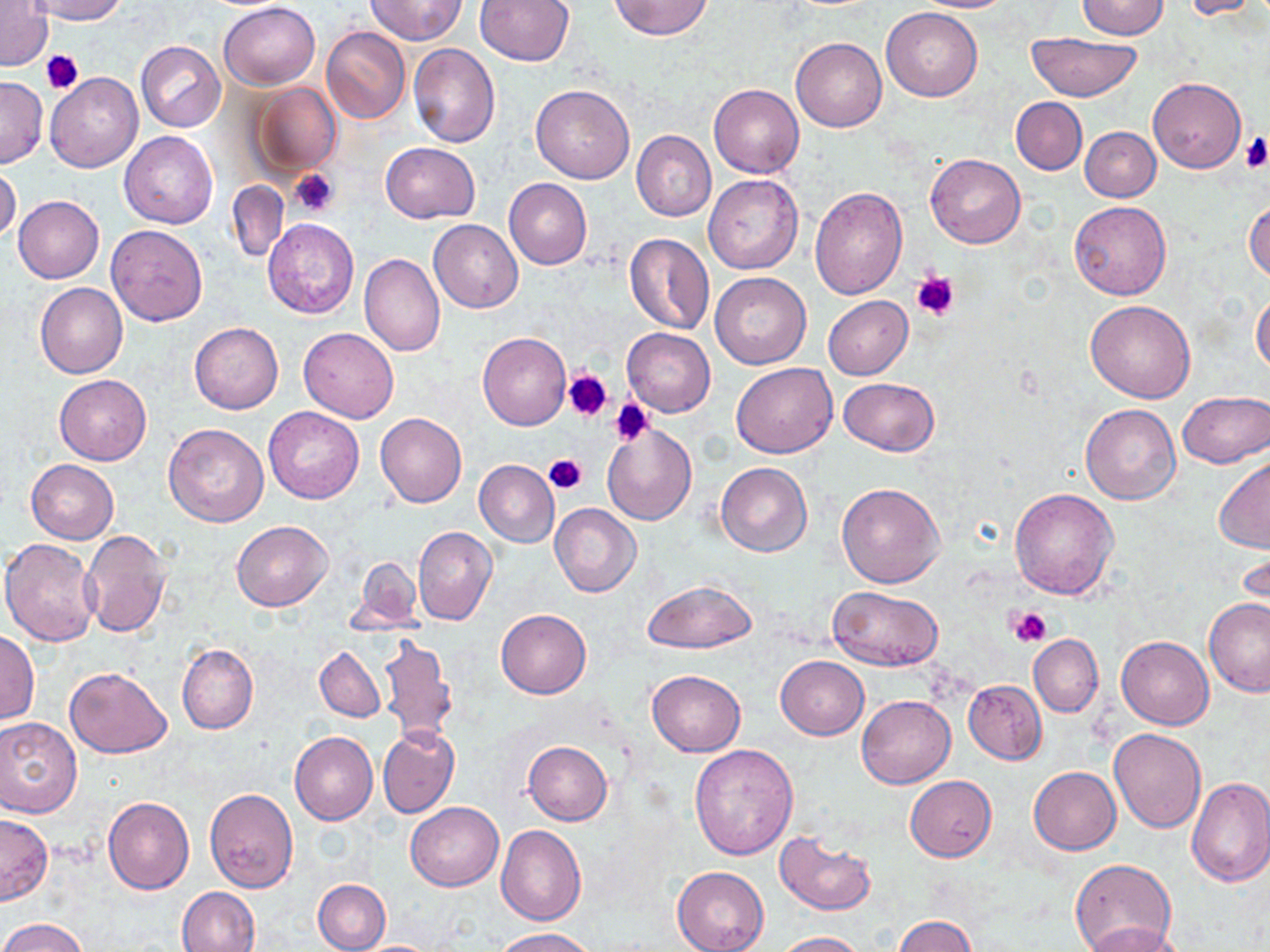

Summary:
  - Coordinate format: approximate bounding boxes as (x1,y1)-(x2,y2) corner pairs in pixels
  - Uninfected red blood cell locations: (23,0)-(128,24), (365,0)-(468,45), (474,0)-(575,66), (911,0)-(1014,12), (1075,0)-(1169,40), (1178,0)-(1264,19), (609,1)-(713,39), (1,2)-(53,73), (219,3)-(320,90), (883,8)-(982,101), (321,26)-(411,124), (1025,32)-(1142,100), (791,37)-(887,132), (135,40)-(226,132), (408,44)-(500,148), (44,73)-(142,173), (0,76)-(47,167), (1148,77)-(1245,172), (250,83)-(340,177), (531,83)-(634,183), (710,84)-(804,178), (1010,97)-(1086,174), (1081,127)-(1161,201), (119,131)-(218,228), (631,131)-(716,221), (380,142)-(482,224), (926,153)-(1026,249), (0,165)-(21,244), (705,175)-(804,275), (504,178)-(591,270), (226,180)-(288,263), (810,185)-(908,299), (14,195)-(104,283), (1245,198)-(1270,284), (1068,200)-(1172,300), (263,217)-(360,318), (428,218)-(523,312), (105,225)-(208,326), (624,233)-(714,335), (359,254)-(445,357), (709,271)-(812,370), (36,282)-(128,378), (1252,290)-(1270,377), (823,296)-(912,379), (1085,299)-(1196,403), (190,323)-(283,414), (298,328)-(398,422), (623,328)-(716,416), (478,331)-(571,430), (732,362)-(838,457), (53,374)-(152,465), (838,377)-(938,457), (1178,390)-(1270,468), (1080,404)-(1181,505), (263,407)-(364,504), (375,412)-(466,508), (163,422)-(269,527), (602,424)-(697,525), (1215,456)-(1270,551), (25,459)-(119,543), (474,460)-(559,546), (715,462)-(812,558), (836,483)-(945,588), (1009,487)-(1121,599), (550,503)-(642,597), (231,521)-(332,611), (413,526)-(497,625), (80,529)-(172,638), (2,537)-(102,646), (1237,542)-(1269,629), (353,557)-(424,630), (643,579)-(756,654), (828,587)-(942,671), (1203,597)-(1270,695), (495,609)-(591,699), (0,631)-(38,724), (1028,634)-(1103,716), (378,635)-(457,746), (1115,635)-(1213,731), (178,645)-(258,734), (315,645)-(386,722), (775,655)-(868,739), (64,666)-(172,757), (647,670)-(745,756), (963,680)-(1046,763), (857,695)-(955,788), (0,717)-(82,816), (377,726)-(460,819), (1108,728)-(1205,833), (290,731)-(378,825), (523,742)-(612,825), (689,743)-(798,861), (1029,767)-(1120,854), (904,776)-(996,861), (1186,776)-(1270,888), (204,788)-(298,893), (103,796)-(194,895), (405,802)-(503,890), (0,814)-(52,905), (497,824)-(586,926), (774,831)-(878,916), (1069,859)-(1176,952), (672,866)-(769,952), (313,878)-(390,951), (178,886)-(260,951), (892,915)-(977,952), (2,918)-(89,952), (1081,922)-(1188,952), (495,927)-(597,951), (771,931)-(868,951), (353,940)-(443,951)
  - Platelet locations: (40,50)-(83,93), (1242,133)-(1270,174), (288,168)-(338,217), (910,269)-(961,321), (563,369)-(613,422), (608,398)-(653,446), (544,453)-(587,493), (1009,608)-(1049,646)
  - Slide-level diagnosis: negative for blood parasites
  - Modality: light microscopy
  - Image size: 1270×952 pixels
  - Field of view: single
  - Magnification: 1000x
  - Preparation: thin blood smear
  - Stain: May-Grünwald-Giemsa